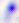
Summary:
  - Identification: Toxoplasma gondii
  - Modality: micrograph
  - Magnification: 400x